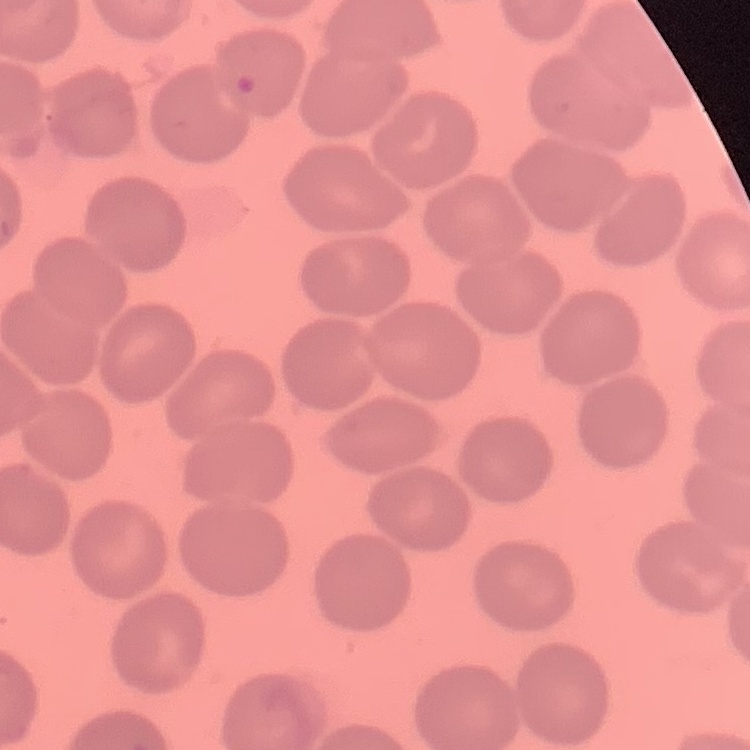
Summary:
  - Erythrocyte morphology: no rouleaux formation
  - Image type: square crop of a larger photomicrograph
  - Stain: Field's or Giemsa
  - Preparation: thin blood smear